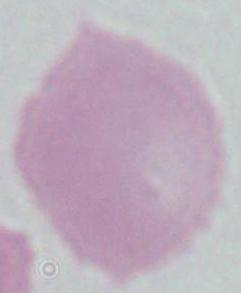

Summary:
  - Modality: photomicrograph
  - Identification: erythrocyte
  - Magnification: 1000x